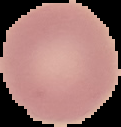 The area outside the segmented cell region is set to black. Malaria status: uninfected. Image is 121×127 pixels. From a thin blood film.